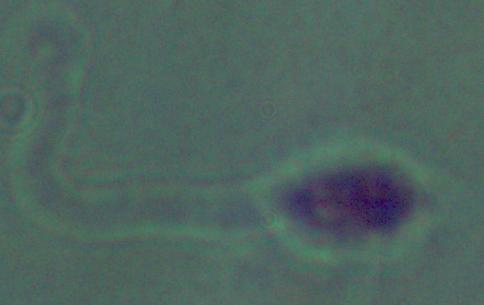
Summary:
  - Magnification: 1000x
  - Modality: micrograph
  - Identification: Leishmania